State which parasite is depicted.
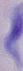

This is a trypanosome.

modality = photomicrograph
magnification = 1000x